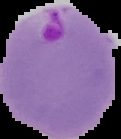
From a thin blood film. Image is 121×139 pixels. The area outside the segmented cell region is set to black. Result: malaria parasites identified.